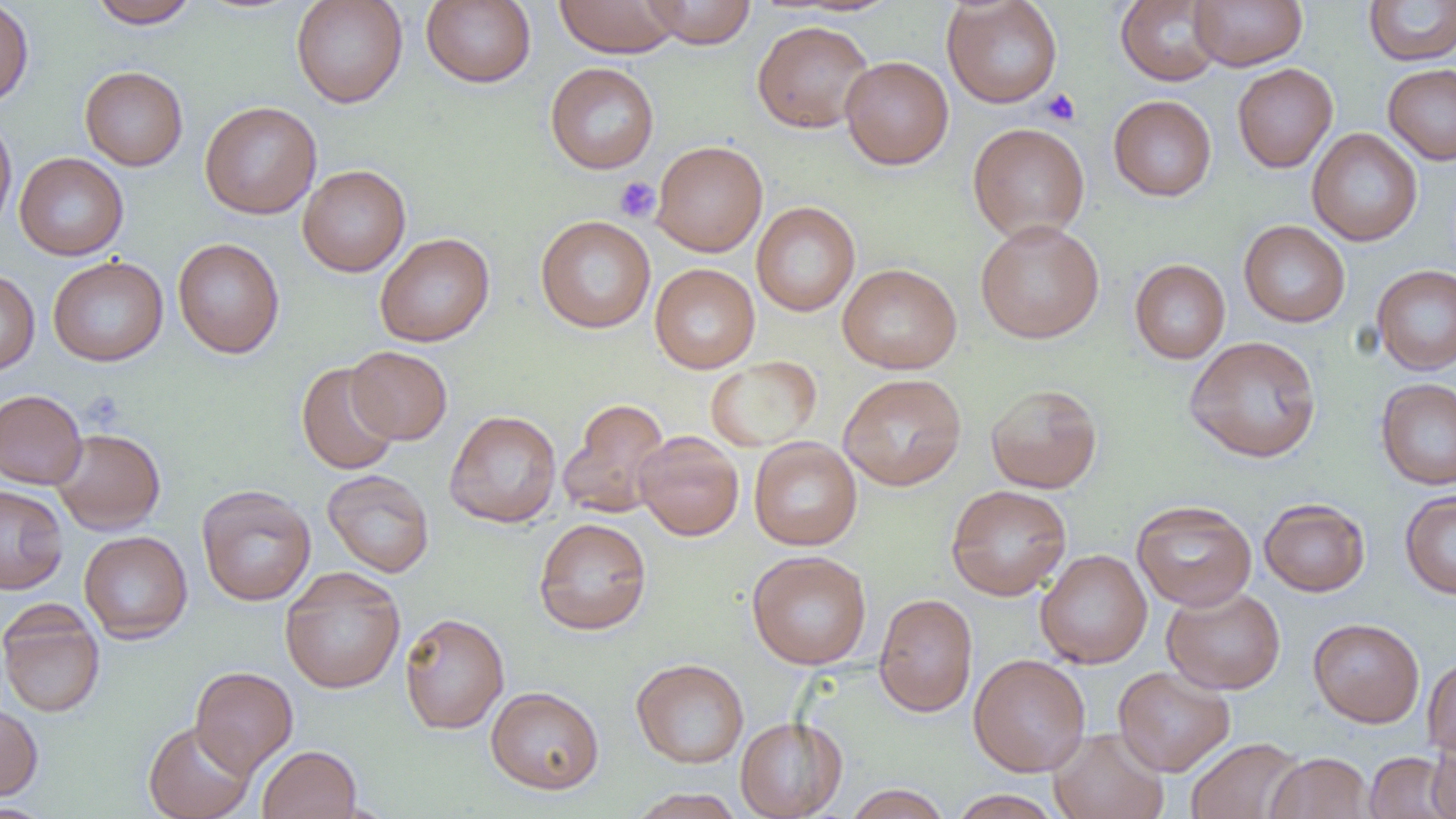

Approximate bounding boxes as named x1/y1/x2/y2 corners in pixels. Platelet locations: (x1=1041, y1=88, x2=1080, y2=126), (x1=614, y1=176, x2=661, y2=223), (x1=81, y1=390, x2=125, y2=431). Uninfected red blood cell locations: (x1=0, y1=0, x2=34, y2=109), (x1=88, y1=0, x2=200, y2=29), (x1=291, y1=0, x2=408, y2=108), (x1=421, y1=0, x2=536, y2=88), (x1=641, y1=0, x2=757, y2=48), (x1=942, y1=0, x2=1063, y2=108), (x1=1116, y1=0, x2=1225, y2=86), (x1=1189, y1=0, x2=1307, y2=71), (x1=1363, y1=0, x2=1456, y2=66), (x1=554, y1=1, x2=683, y2=57), (x1=752, y1=19, x2=875, y2=133), (x1=840, y1=55, x2=954, y2=170), (x1=545, y1=62, x2=659, y2=174), (x1=1232, y1=63, x2=1338, y2=173), (x1=1383, y1=64, x2=1456, y2=165), (x1=80, y1=66, x2=188, y2=171), (x1=1108, y1=95, x2=1216, y2=201), (x1=199, y1=101, x2=322, y2=219), (x1=0, y1=113, x2=17, y2=235), (x1=968, y1=123, x2=1090, y2=242), (x1=1307, y1=128, x2=1422, y2=246), (x1=651, y1=140, x2=768, y2=257), (x1=14, y1=152, x2=128, y2=260), (x1=298, y1=164, x2=411, y2=277), (x1=751, y1=201, x2=860, y2=316), (x1=535, y1=215, x2=656, y2=333), (x1=975, y1=219, x2=1105, y2=343), (x1=1239, y1=220, x2=1351, y2=327), (x1=374, y1=232, x2=495, y2=347), (x1=172, y1=237, x2=285, y2=359), (x1=48, y1=256, x2=168, y2=366), (x1=1130, y1=259, x2=1230, y2=364), (x1=650, y1=263, x2=760, y2=373), (x1=837, y1=263, x2=962, y2=374), (x1=1371, y1=264, x2=1456, y2=375), (x1=0, y1=269, x2=40, y2=375), (x1=1184, y1=335, x2=1322, y2=463), (x1=346, y1=346, x2=453, y2=444), (x1=705, y1=356, x2=822, y2=452), (x1=295, y1=361, x2=400, y2=475), (x1=838, y1=372, x2=967, y2=491), (x1=1376, y1=377, x2=1456, y2=490), (x1=985, y1=383, x2=1102, y2=494), (x1=0, y1=389, x2=87, y2=489), (x1=558, y1=399, x2=672, y2=519), (x1=444, y1=410, x2=562, y2=528), (x1=51, y1=428, x2=165, y2=534), (x1=635, y1=431, x2=745, y2=541), (x1=749, y1=437, x2=862, y2=550), (x1=322, y1=469, x2=435, y2=578), (x1=0, y1=484, x2=68, y2=594), (x1=945, y1=484, x2=1072, y2=600), (x1=196, y1=485, x2=316, y2=606), (x1=1400, y1=490, x2=1456, y2=599), (x1=1259, y1=498, x2=1371, y2=597), (x1=1131, y1=499, x2=1257, y2=611), (x1=533, y1=517, x2=652, y2=635), (x1=79, y1=530, x2=193, y2=643), (x1=1036, y1=549, x2=1152, y2=669), (x1=746, y1=550, x2=872, y2=669), (x1=279, y1=567, x2=406, y2=694), (x1=1162, y1=586, x2=1286, y2=694), (x1=873, y1=592, x2=978, y2=717), (x1=0, y1=602, x2=105, y2=718), (x1=399, y1=612, x2=510, y2=734), (x1=1308, y1=618, x2=1425, y2=727), (x1=968, y1=654, x2=1091, y2=777), (x1=1422, y1=655, x2=1456, y2=758), (x1=631, y1=658, x2=749, y2=769), (x1=190, y1=666, x2=298, y2=776), (x1=1112, y1=666, x2=1235, y2=776), (x1=485, y1=686, x2=605, y2=794), (x1=0, y1=702, x2=43, y2=801), (x1=735, y1=716, x2=847, y2=819), (x1=143, y1=720, x2=256, y2=819), (x1=1048, y1=727, x2=1169, y2=819), (x1=1428, y1=730, x2=1456, y2=817), (x1=1186, y1=737, x2=1305, y2=819), (x1=257, y1=745, x2=362, y2=818), (x1=1364, y1=751, x2=1453, y2=819), (x1=1264, y1=752, x2=1374, y2=818), (x1=844, y1=784, x2=953, y2=818), (x1=628, y1=788, x2=746, y2=819), (x1=949, y1=789, x2=1062, y2=819), (x1=1, y1=802, x2=53, y2=818). Slide-level diagnosis: no evidence of blood parasites. Light microscopy. Image is 1456×819 pixels. Thin blood film. Captured at 1000x magnification. One field of a larger specimen.